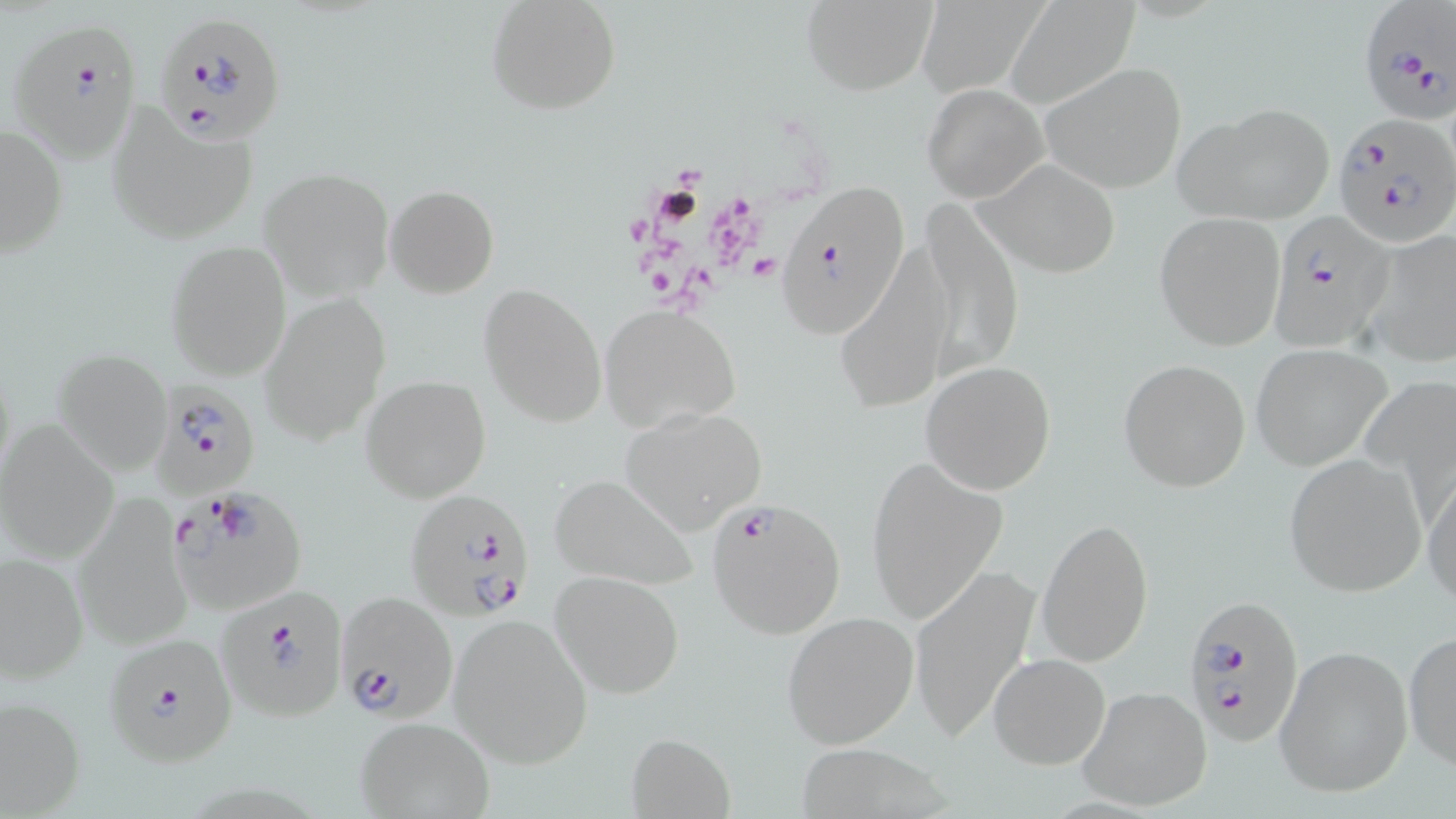

Summary:
  - Coordinate format: approximate bounding boxes as named x1/y1/x2/y2 corners in pixels
  - Plasmodium falciparum-infected red blood cell locations: (x1=1355, y1=2, x2=1455, y2=126), (x1=154, y1=11, x2=286, y2=143), (x1=8, y1=21, x2=143, y2=162), (x1=1333, y1=113, x2=1456, y2=243), (x1=774, y1=179, x2=915, y2=341), (x1=1271, y1=210, x2=1393, y2=355), (x1=154, y1=381, x2=259, y2=500), (x1=405, y1=487, x2=535, y2=620), (x1=170, y1=493, x2=307, y2=614), (x1=707, y1=497, x2=847, y2=640), (x1=215, y1=584, x2=349, y2=721), (x1=333, y1=590, x2=459, y2=726), (x1=1182, y1=592, x2=1306, y2=748), (x1=103, y1=633, x2=237, y2=767)
  - Uninfected red blood cell locations: (x1=486, y1=0, x2=621, y2=116), (x1=799, y1=0, x2=937, y2=95), (x1=918, y1=0, x2=1045, y2=97), (x1=1005, y1=0, x2=1140, y2=110), (x1=1040, y1=61, x2=1190, y2=194), (x1=922, y1=84, x2=1047, y2=201), (x1=1175, y1=101, x2=1335, y2=225), (x1=105, y1=102, x2=263, y2=244), (x1=1, y1=122, x2=69, y2=258), (x1=976, y1=157, x2=1123, y2=277), (x1=261, y1=167, x2=396, y2=301), (x1=385, y1=184, x2=498, y2=299), (x1=917, y1=202, x2=1023, y2=379), (x1=1155, y1=213, x2=1287, y2=350), (x1=1360, y1=230, x2=1456, y2=367), (x1=165, y1=240, x2=292, y2=380), (x1=832, y1=242, x2=952, y2=415), (x1=479, y1=284, x2=606, y2=427), (x1=260, y1=292, x2=390, y2=447), (x1=598, y1=305, x2=742, y2=432), (x1=1250, y1=343, x2=1394, y2=470), (x1=54, y1=346, x2=171, y2=474), (x1=1119, y1=359, x2=1251, y2=492), (x1=920, y1=361, x2=1059, y2=494), (x1=362, y1=374, x2=491, y2=502), (x1=618, y1=410, x2=766, y2=537), (x1=0, y1=421, x2=121, y2=564), (x1=1284, y1=453, x2=1427, y2=597), (x1=865, y1=456, x2=1006, y2=625), (x1=1423, y1=467, x2=1456, y2=607), (x1=549, y1=473, x2=698, y2=591), (x1=73, y1=498, x2=192, y2=650), (x1=1035, y1=518, x2=1154, y2=665), (x1=1, y1=553, x2=89, y2=682), (x1=907, y1=563, x2=1039, y2=743), (x1=551, y1=570, x2=686, y2=699), (x1=781, y1=610, x2=920, y2=749), (x1=448, y1=612, x2=594, y2=770), (x1=1403, y1=629, x2=1456, y2=772), (x1=1273, y1=644, x2=1414, y2=799), (x1=988, y1=654, x2=1110, y2=770), (x1=1078, y1=685, x2=1214, y2=812), (x1=0, y1=694, x2=87, y2=816), (x1=353, y1=716, x2=497, y2=819), (x1=624, y1=732, x2=739, y2=817)
  - Platelet locations: (x1=749, y1=254, x2=780, y2=282)
  - Slide-level diagnosis: Plasmodium falciparum
  - Image size: 1456×819 pixels
  - Stain: May-Grünwald-Giemsa
  - Modality: light microscopy
  - Magnification: 1000x
  - Preparation: thin blood smear
  - Field of view: one of a larger specimen